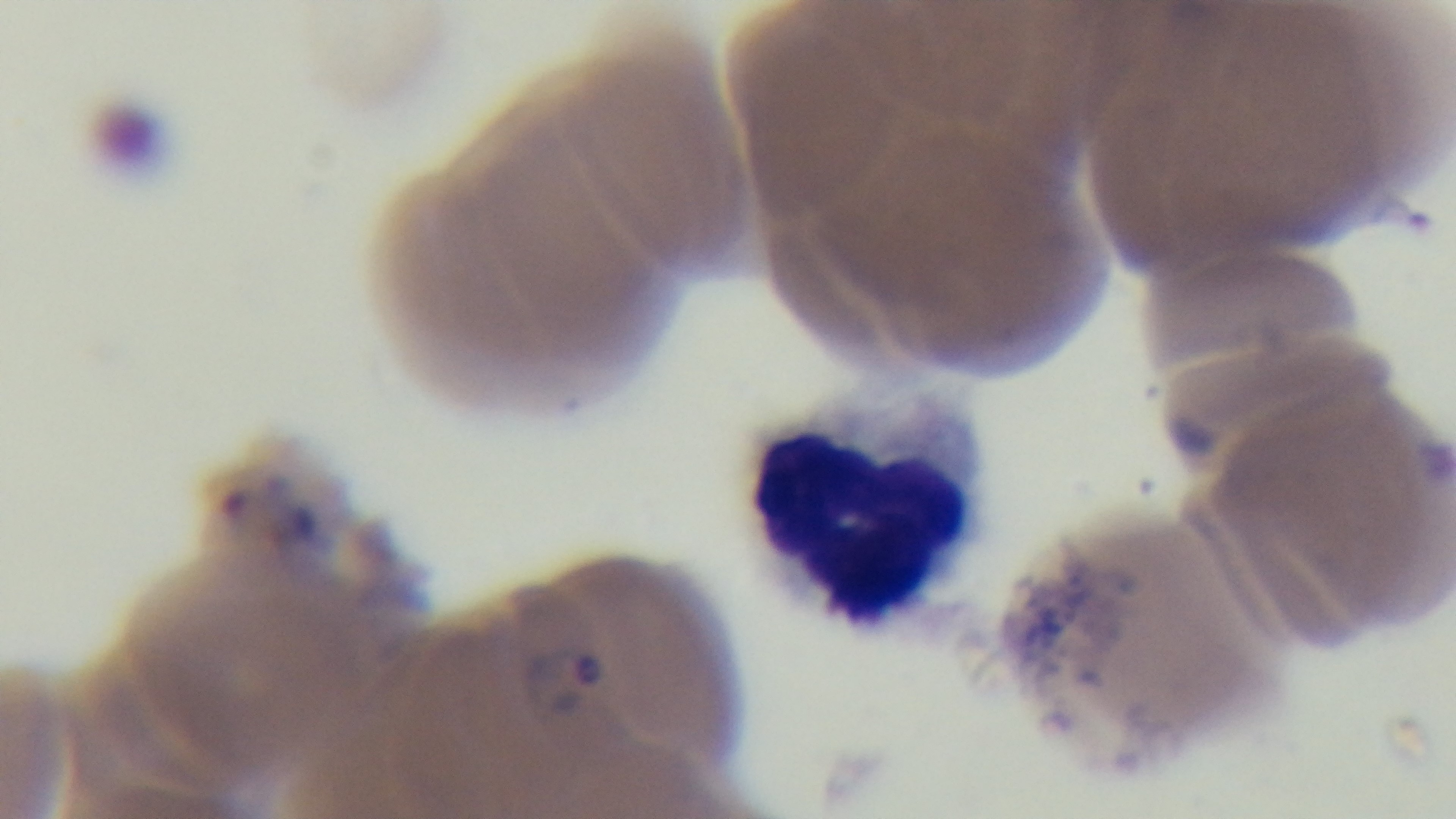

malaria status = positive
objective = 100x oil immersion
modality = light microscopy
field of view = one from the slide
preparation = thin
stain = Giemsa
capture = mounted 4K digital camera